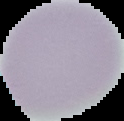

Cell region segmented out of the field of view; the surrounding area is masked to black. Malaria status: uninfected. Image is 124×121 pixels. From a thin blood smear.